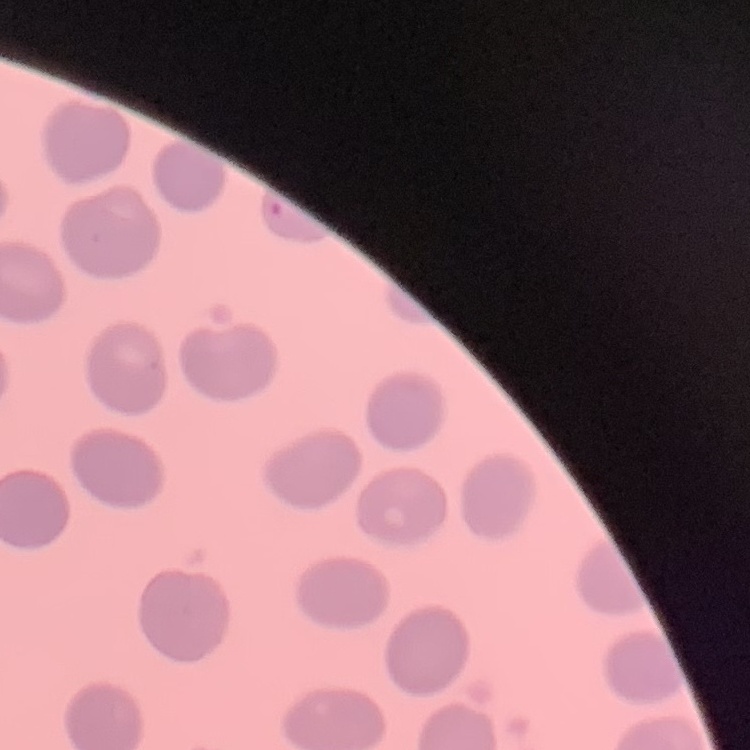 The erythrocytes exhibit no rouleaux formation. One tile cut from a larger photomicrograph. Field's or Giemsa stain. Thin blood film.